Classify this cell by malaria status.
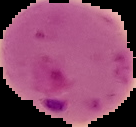
It is parasitized.

Summary:
  - Image size: 136×127 pixels
  - Preparation: thin blood smear
  - Image type: segmented cell region on a black background